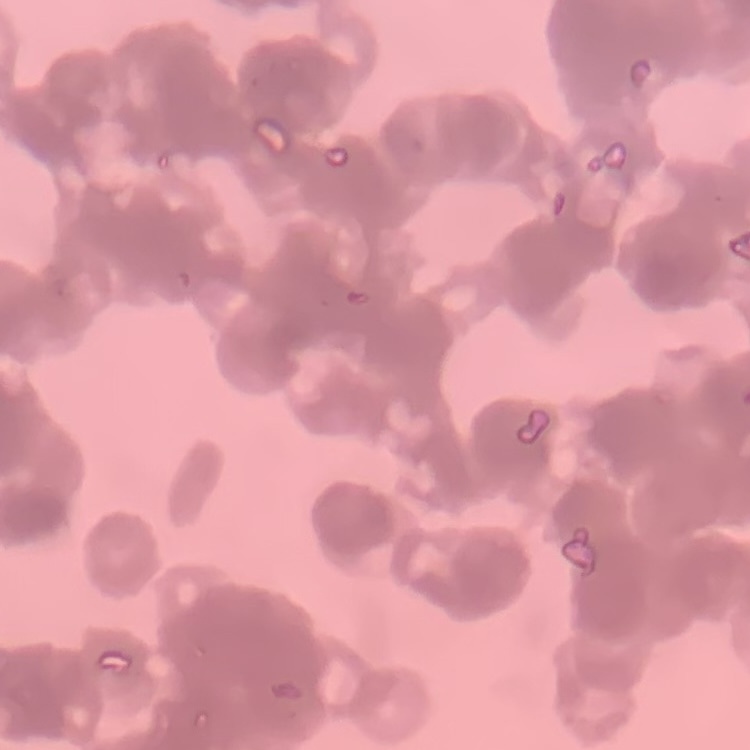 The red blood cells exhibit rouleaux formation. Thin peripheral smear. Stained with either Field's or Giemsa. One tile cut from a larger photomicrograph.